Report the malaria status of this cell.
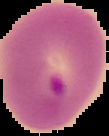
Parasitized.

{
  "image_type": "cell region segmented out of the field of view; surrounding area masked to black",
  "image_size": "109×136 pixels",
  "preparation": "thin blood smear"
}